Classify this cell by malaria status.
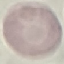
It is uninfected.

preparation = thin blood smear
image type = automatically extracted cell patch, resized to 64 × 64 pixels
capture = smartphone camera at the microscope eyepiece
stain = Giemsa